Name the parasite shown.
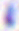

This is Toxoplasma gondii.

Summary:
  - Magnification: 400x
  - Modality: micrograph